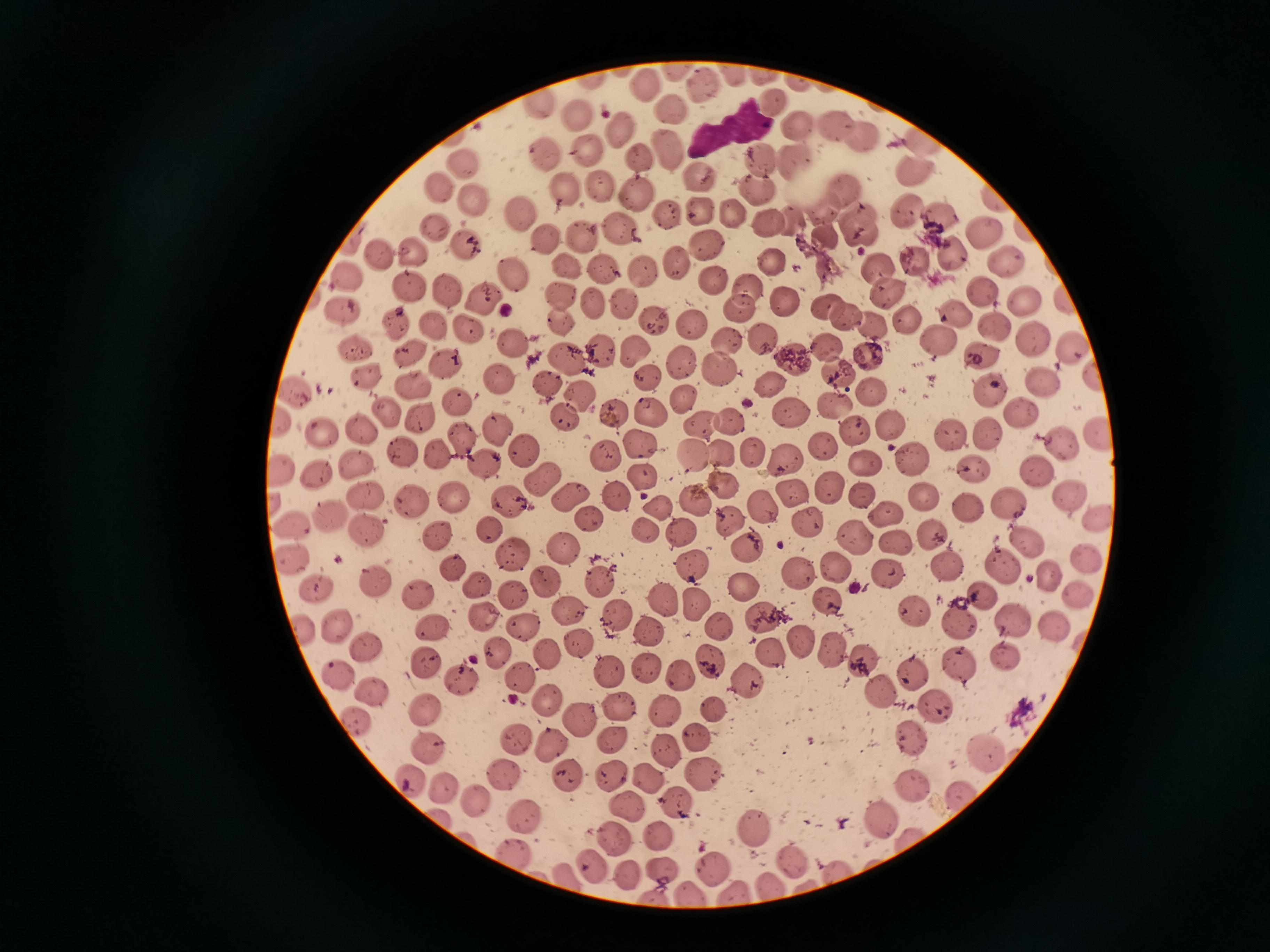 Approximate centers as [x, y] in pixels. Cell locations: [642, 84], [704, 86], [772, 100], [675, 106], [579, 114], [836, 120], [796, 123], [621, 132], [860, 135], [668, 146], [590, 149], [759, 158], [546, 159], [644, 159], [796, 159], [465, 165], [914, 170], [698, 179], [603, 188], [440, 189], [567, 189], [754, 189], [845, 191], [637, 194], [474, 201], [699, 210], [904, 212], [520, 214], [670, 214], [736, 217], [942, 220], [770, 223], [861, 223], [433, 226], [622, 226], [585, 234], [984, 237], [549, 240], [707, 244], [465, 246], [415, 249], [378, 252], [949, 254], [676, 261], [770, 261], [1006, 262], [567, 267], [878, 267], [599, 269], [641, 269], [518, 276], [714, 276], [408, 285], [745, 286], [888, 290], [983, 290], [452, 291], [564, 294], [485, 298], [789, 302], [1025, 302], [625, 304], [598, 305], [830, 305], [744, 306], [957, 311], [847, 319], [906, 319], [652, 321], [560, 322], [395, 323], [690, 323], [873, 323], [432, 325], [991, 326], [465, 327], [767, 339], [940, 339], [1033, 340], [724, 342], [517, 344], [1071, 344], [824, 345], [636, 348], [354, 350], [602, 351], [983, 353], [566, 355], [869, 355], [446, 358], [793, 358], [679, 363], [721, 367], [835, 372], [370, 373], [644, 379], [500, 382], [1041, 382], [544, 383], [769, 383], [412, 385], [994, 388], [870, 390], [297, 391], [683, 396], [584, 397], [453, 401], [836, 403], [1024, 408], [613, 409], [792, 410], [652, 412], [388, 414], [565, 416], [422, 418], [729, 420], [697, 423], [889, 423], [321, 428], [360, 429], [499, 431], [857, 432], [950, 432], [1094, 432], [989, 435], [462, 438], [640, 443], [1065, 446], [405, 449], [750, 449], [822, 449], [524, 451], [727, 452], [437, 455], [692, 455], [784, 459], [916, 459], [605, 460], [482, 462], [870, 463], [361, 464], [972, 468], [1034, 472], [319, 473], [642, 476], [542, 482], [723, 485], [831, 486], [793, 493], [369, 494], [571, 495], [610, 495], [862, 495], [1069, 495], [926, 496], [455, 497], [509, 499], [689, 500], [409, 501], [1010, 505], [661, 506], [759, 506], [970, 508], [887, 514], [335, 515], [588, 518], [1099, 518], [806, 523], [293, 527], [368, 528], [488, 528], [647, 532], [684, 532], [930, 533], [439, 536], [849, 538], [1029, 539], [899, 544], [745, 546], [563, 548], [512, 555], [292, 557], [1086, 560], [1003, 564], [456, 565], [693, 565], [798, 567], [951, 568], [837, 572], [889, 575], [1050, 576], [378, 578], [603, 582], [313, 584], [476, 584], [742, 586], [981, 591], [514, 595], [1079, 595], [417, 596], [661, 597], [826, 602], [696, 604], [909, 607], [620, 616], [763, 616], [483, 618], [960, 622], [720, 623], [1017, 623], [340, 625], [1052, 626], [429, 627], [524, 627], [649, 629], [796, 640], [579, 641], [370, 644], [833, 648], [496, 652], [771, 654], [543, 655], [1005, 656], [428, 662], [859, 662], [713, 663], [647, 666], [956, 666], [608, 673], [913, 673], [680, 674], [519, 676], [338, 678], [746, 678], [464, 683], [881, 692], [376, 695], [545, 700], [618, 705], [937, 705], [421, 709], [715, 710], [665, 712], [582, 720], [909, 734], [696, 736], [512, 739], [611, 739], [552, 745], [429, 746], [984, 747], [667, 751], [503, 772], [608, 773], [647, 775], [568, 777], [406, 778], [700, 779], [914, 783], [446, 791], [955, 793], [677, 800], [474, 805], [627, 806], [529, 817], [882, 820], [753, 826], [659, 835], [619, 839], [513, 848], [790, 861], [593, 863], [713, 867], [658, 869], [630, 877], [771, 884]. Photographed with a smartphone camera at the microscope eyepiece. Image is 1270×952 pixels. One field from this slide. Thin smear of blood. Giemsa-stained preparation.